Identify the parasite.
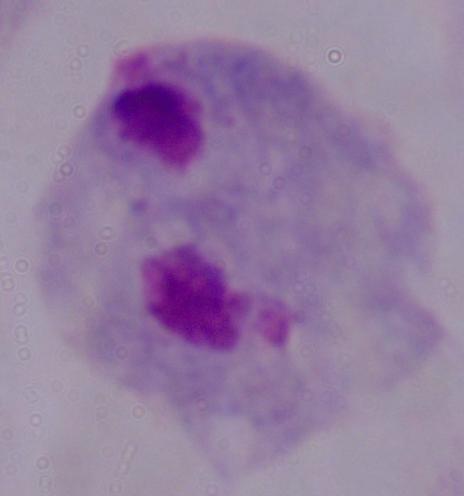

A trichomonad.

Captured at 1000x magnification. Photomicrograph.